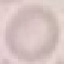
Summary:
  - Malaria status: uninfected
  - Stain: Giemsa
  - Capture: smartphone camera at the microscope eyepiece
  - Image type: cell patch, automatically extracted from a larger field of view and resized to 64 × 64 pixels
  - Preparation: thin smear